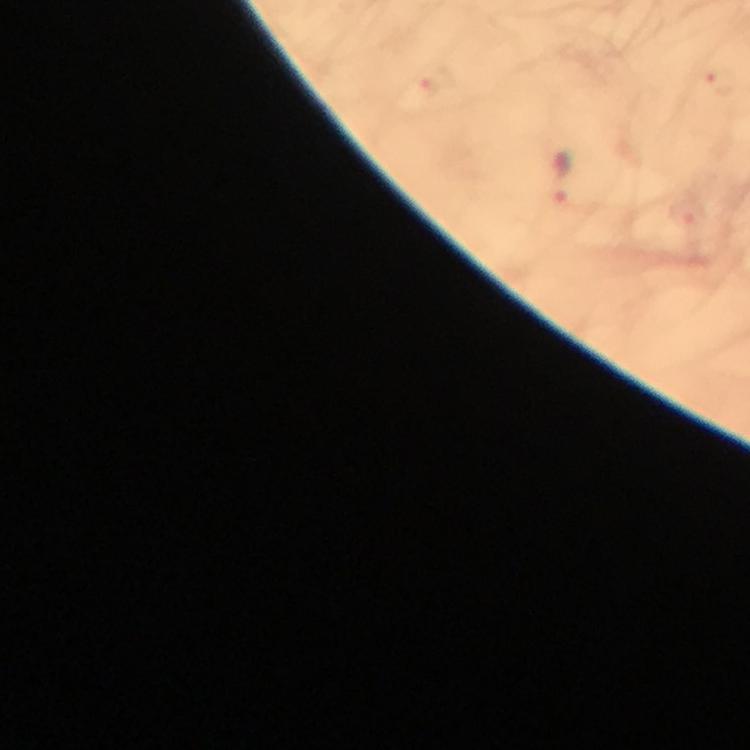
{
  "preparation": "thick smear",
  "immersion_oil": "used",
  "magnification": "100x",
  "stain": "Giemsa",
  "cropped_from": "a single field of view",
  "image_size": "750×750 pixels",
  "capture": "smartphone camera through the microscope",
  "plasmodium_parasite_locations": "approximate object centers, in pixels from the top-left corner: (x=562, y=177)",
  "context": "from a malaria diagnostic workup"
}